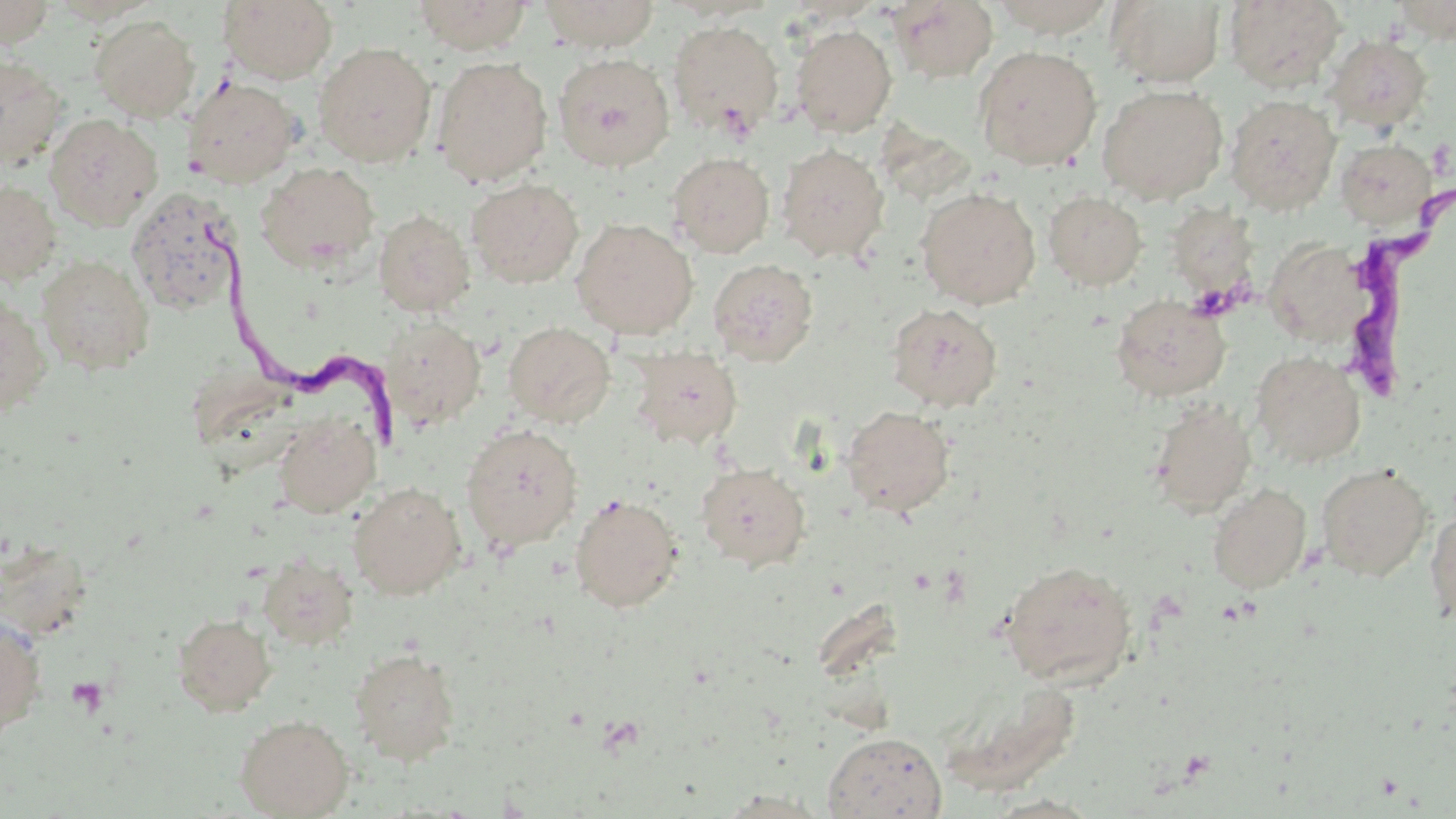
Approximate bounding boxes as (x1,y1)-(x2,y2) corner pairs in pixels. Platelet locations: (66,676)-(109,717). Trypanosoma brucei locations: (1330,188)-(1455,410), (188,222)-(403,450). Uninfected red blood cell locations: (0,0)-(56,47), (412,0)-(533,54), (540,0)-(660,52), (889,0)-(999,83), (987,0)-(1119,37), (1224,0)-(1346,91), (1389,0)-(1456,42), (219,1)-(339,84), (1106,1)-(1226,87), (90,15)-(200,122), (668,20)-(784,139), (790,24)-(897,136), (1325,35)-(1433,133), (313,42)-(437,167), (973,45)-(1102,170), (553,52)-(675,172), (0,55)-(67,169), (432,56)-(553,186), (181,76)-(303,188), (1097,84)-(1228,204), (1226,94)-(1341,214), (44,114)-(163,230), (1335,138)-(1439,230), (776,143)-(890,263), (667,152)-(774,258), (255,161)-(380,271), (467,178)-(584,288), (0,180)-(61,284), (126,186)-(244,317), (916,187)-(1041,308), (1044,190)-(1148,291), (373,209)-(475,317), (571,217)-(698,339), (1263,236)-(1371,348), (37,254)-(155,375), (707,258)-(818,366), (1110,294)-(1230,402), (0,296)-(53,417), (885,302)-(1003,412), (381,317)-(486,430), (502,321)-(616,428), (629,347)-(743,450), (1250,350)-(1366,467), (1145,399)-(1257,517), (841,405)-(956,516), (273,412)-(381,518), (460,423)-(584,553), (696,462)-(811,572), (1315,463)-(1433,581), (348,481)-(467,600), (1207,483)-(1311,593), (569,493)-(683,613), (1424,504)-(1456,629), (258,553)-(359,650), (999,558)-(1138,687), (0,611)-(47,741), (172,613)-(277,716), (349,647)-(461,765), (235,714)-(353,818), (822,731)-(947,818), (714,789)-(834,817), (983,793)-(1105,817). Slide-level diagnosis: Trypanosoma brucei. Optical microscopy. Image is 1456×819 pixels. May-Grünwald-Giemsa-stained preparation. Thin blood smear. Single field of view. Captured at 1000x magnification.